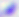
Summary:
  - Identification: Toxoplasma gondii
  - Modality: micrograph
  - Magnification: 400x